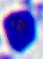
identification = white blood cell
modality = photomicrograph
magnification = 400x